Identify the parasite.
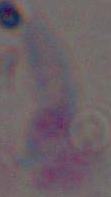

This is Toxoplasma gondii.

Micrograph. Captured at 1000x magnification.